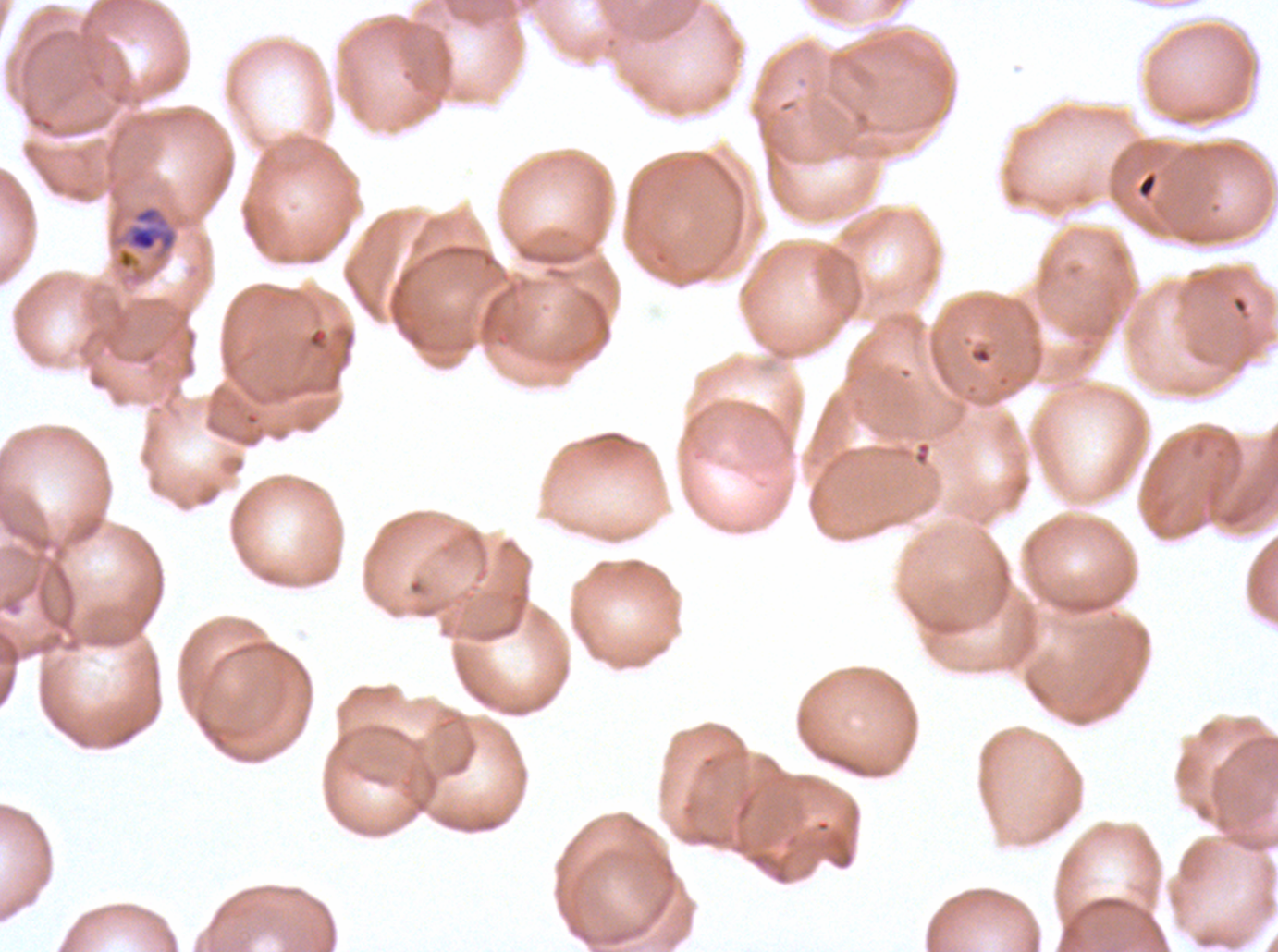 Approximate bounding rectangles given as corner coordinates in pixels from the top-left. Mid trophozoite locations: (x1=127, y1=206, x2=177, y2=252). P. falciparum from a patient in The Gambia, cultured ex vivo for 24 to 48 hours. Giemsa stain. Image is 1278×952 pixels. Thin blood smear. A sub-image separated from a larger composite.